Comment on the morphology of the erythrocytes.
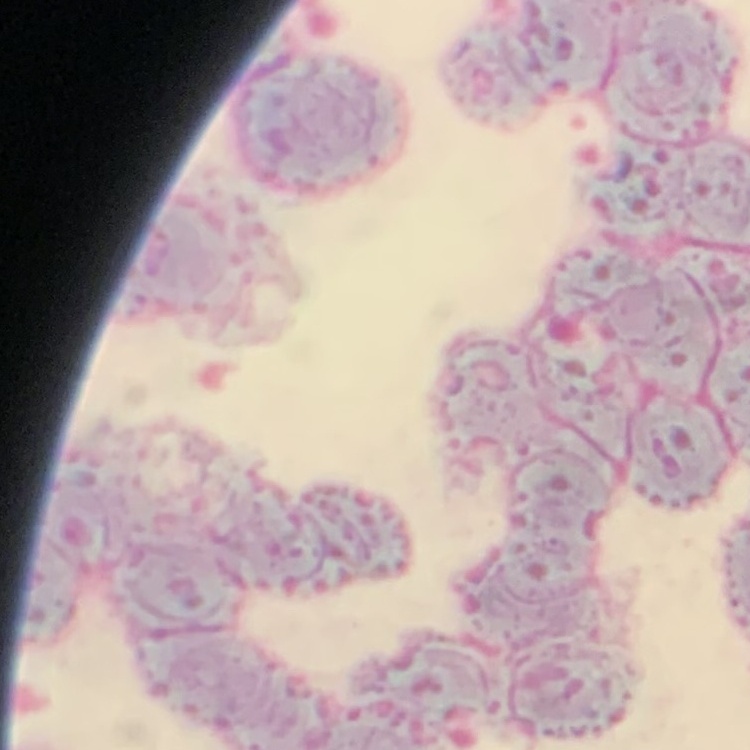
Rouleaux formation.

Summary:
  - Image type: one tile cut from a larger photomicrograph
  - Preparation: thin blood film
  - Stain: Field's or Giemsa